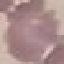

result = negative for malaria parasites
capture = smartphone through the microscope eyepiece
preparation = thin blood film
stain = Giemsa
image type = cell patch, automatically extracted from a larger field of view and resized to 64 × 64 pixels